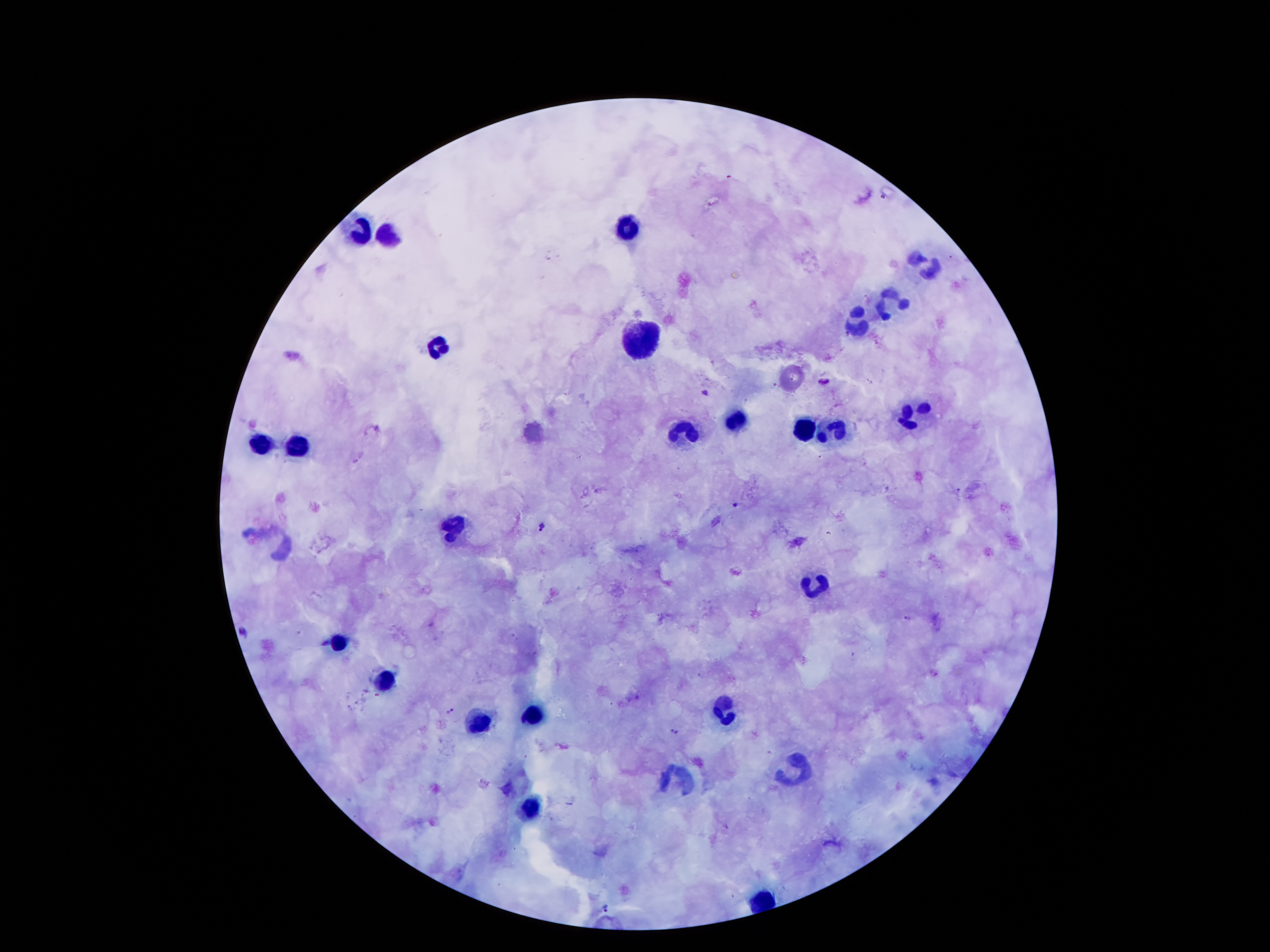

Approximate centers as [x, y] in pixels. Malaria parasite locations: [824, 382], [706, 393], [736, 505], [543, 528], [908, 618], [245, 632], [453, 712], [674, 731], [604, 906]. Leukocyte locations: [627, 231], [359, 235], [388, 238], [927, 264], [893, 302], [862, 323], [641, 342], [438, 348], [737, 418], [909, 418], [832, 428], [804, 430], [684, 433], [298, 444], [257, 449], [450, 527], [815, 584], [337, 639], [385, 681], [537, 711], [725, 711], [477, 722], [796, 773], [681, 778], [529, 810]. Giemsa stain. Patient malaria status: infected with Plasmodium falciparum. Image is 1270×952 pixels. Photographed through the microscope eyepiece with a smartphone camera. 100x magnification. Single field of view. Thick peripheral-blood smear.